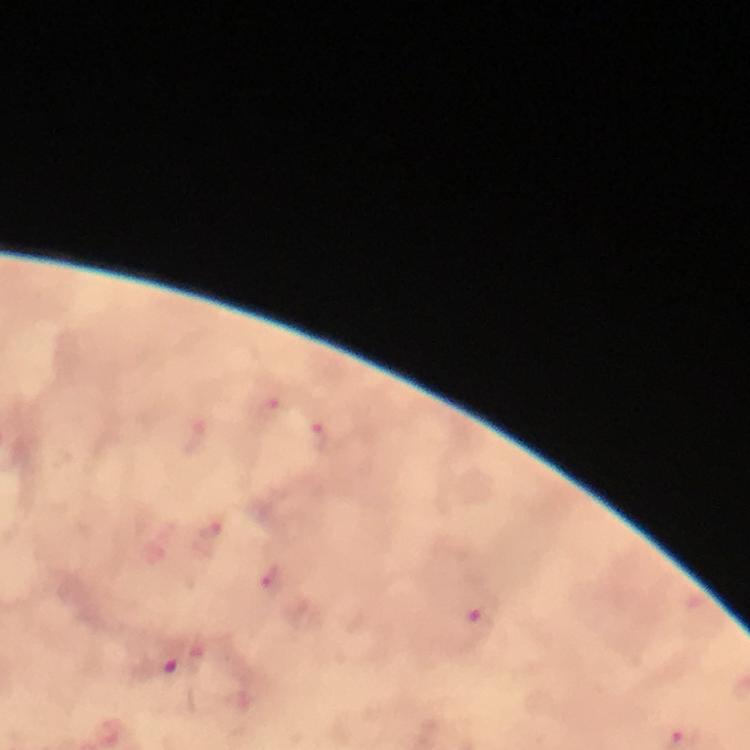

Approximate centers as [x, y] in pixels. Plasmodium parasite locations: [321, 437], [209, 537], [272, 579], [483, 615], [158, 662]. Photographed through the microscope with a smartphone camera. Immersion oil applied. 100x magnification. Thick blood film. From a malaria diagnostic workup. Giemsa stain. A crop from one field of view. Image is 750×750 pixels.